Identify the parasite.
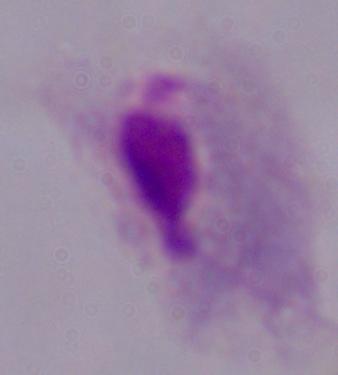
This is a trichomonad.

Summary:
  - Modality: photomicrograph
  - Magnification: 1000x